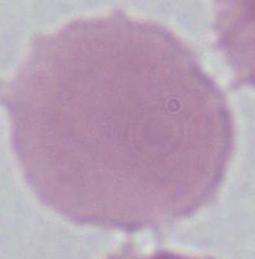 Captured at 1000x magnification. An erythrocyte is shown. Photomicrograph.